Assess this cell for malaria.
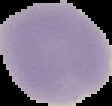

Uninfected.

Summary:
  - Image type: segmented cell region with the area outside set to black
  - Preparation: thin blood smear
  - Image size: 112×106 pixels